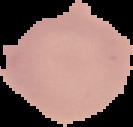

image size = 133×127 pixels
image type = segmented cell region with the area outside set to black
preparation = thin blood smear
result = negative for malaria parasites